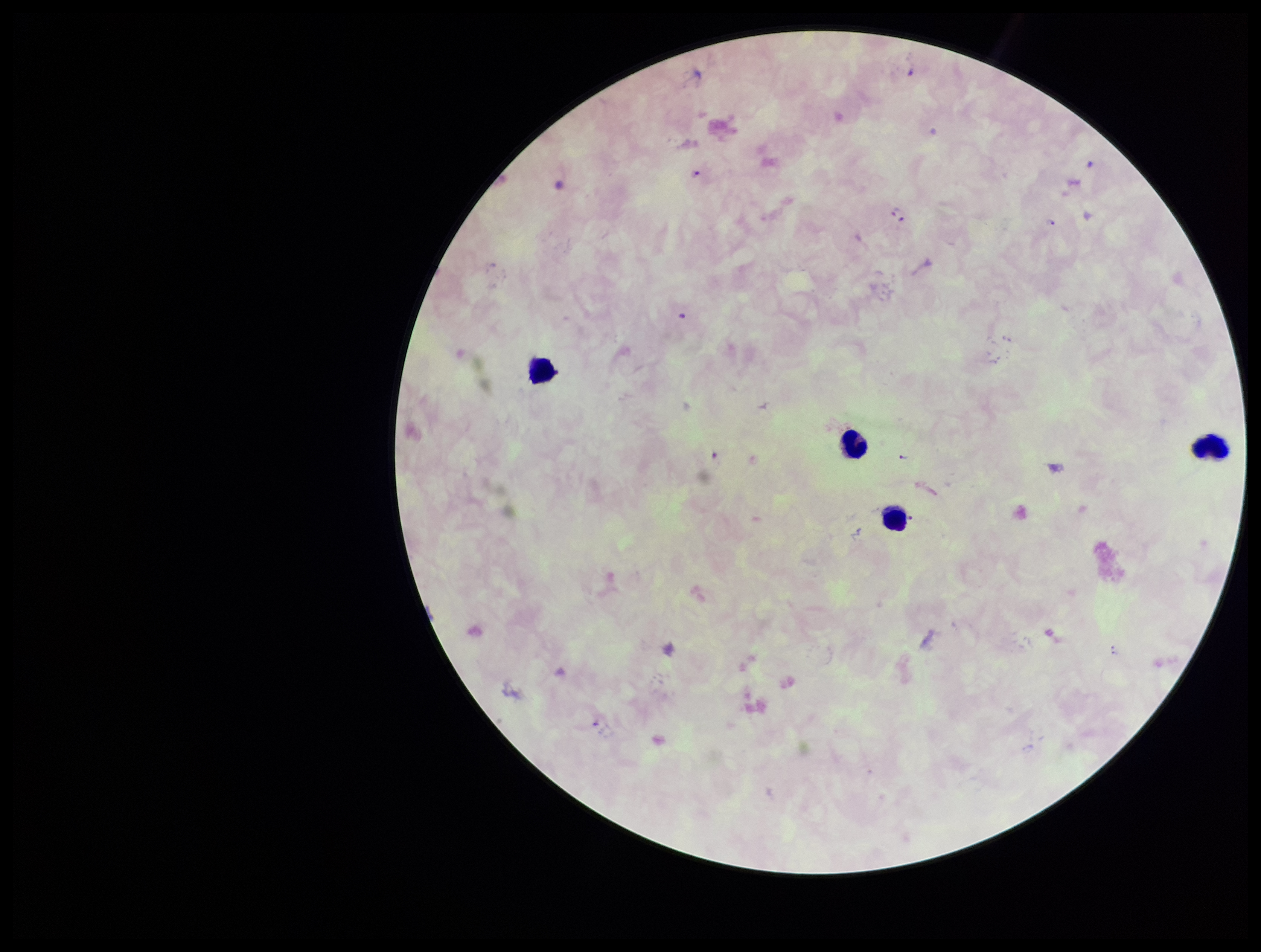
species reported for this patient = Plasmodium falciparum
parasite count = 6
Plasmodium parasites = detected
capture = smartphone photograph through the microscope eyepiece
field of view = single
stain = Giemsa
leukocyte count = 4
preparation = thick blood smear
patient malaria status = infected
image size = 1261×952 pixels